Outline each Trypanosoma brucei.
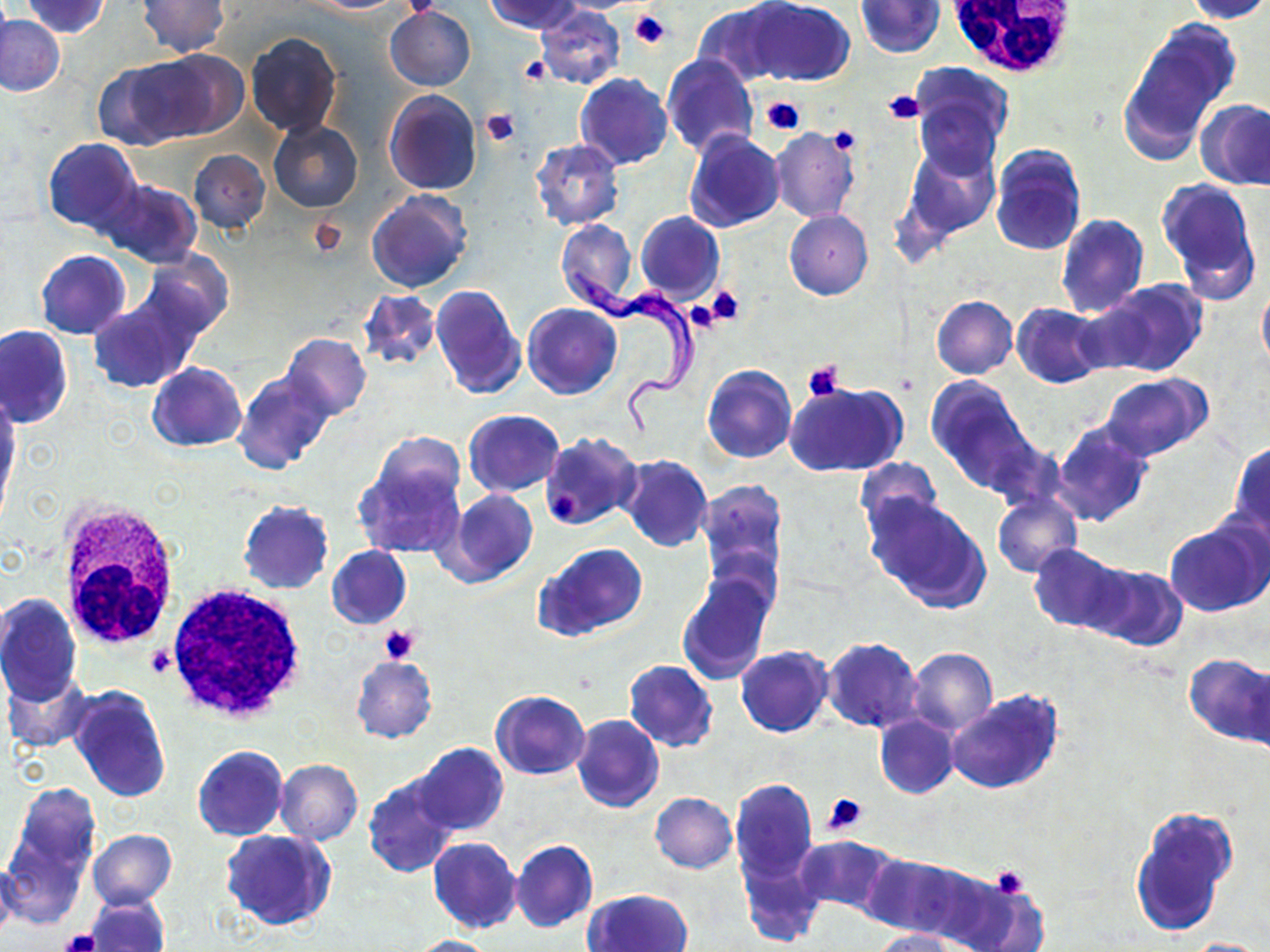
Approximate bounding boxes as [x1, y1, x2, y2] in pixels.
Trypanosoma brucei: [568, 267, 703, 444].

Platelet locations: [629, 7, 672, 50], [518, 56, 550, 85], [881, 89, 926, 124], [761, 96, 804, 136], [480, 108, 518, 147], [826, 126, 861, 156], [705, 285, 744, 327], [801, 359, 846, 402], [379, 625, 421, 666], [147, 645, 178, 679], [824, 792, 867, 834], [988, 865, 1031, 899], [59, 929, 100, 952]. White blood cell locations: [941, 0, 1085, 77], [55, 499, 183, 654], [166, 584, 308, 722]. Uninfected red blood cell locations: [20, 0, 111, 38], [311, 0, 402, 13], [485, 0, 583, 34], [747, 0, 854, 87], [855, 0, 944, 57], [1182, 0, 1270, 24], [137, 1, 230, 56], [694, 1, 793, 88], [535, 6, 625, 90], [624, 6, 674, 58], [385, 7, 475, 90], [1, 15, 65, 97], [1118, 18, 1240, 162], [246, 32, 342, 138], [128, 51, 244, 142], [661, 54, 756, 156], [93, 58, 197, 149], [909, 63, 1014, 155], [574, 73, 673, 171], [384, 89, 482, 194], [1196, 98, 1270, 190], [915, 99, 1001, 181], [268, 120, 364, 212], [770, 127, 860, 223], [684, 128, 785, 233], [42, 138, 141, 236], [531, 139, 624, 231], [901, 142, 1000, 246], [989, 145, 1086, 257], [187, 150, 271, 234], [1156, 179, 1261, 298], [99, 180, 202, 268], [366, 189, 473, 295], [784, 210, 873, 300], [635, 211, 724, 304], [1056, 213, 1148, 317], [556, 219, 639, 311], [35, 250, 130, 338], [138, 251, 231, 341], [1084, 278, 1208, 379], [431, 282, 526, 402], [1256, 283, 1270, 376], [357, 288, 440, 372], [87, 292, 202, 392], [931, 295, 1017, 379], [522, 303, 621, 399], [1012, 303, 1106, 388], [1, 326, 72, 428], [281, 334, 371, 420], [147, 361, 247, 451], [702, 365, 796, 465], [232, 370, 334, 474], [1099, 374, 1210, 462], [925, 378, 1040, 495], [784, 381, 908, 477], [0, 396, 19, 508], [463, 409, 564, 497], [1052, 420, 1153, 528], [540, 431, 642, 529], [370, 433, 466, 517], [1229, 440, 1270, 544], [352, 450, 466, 562], [617, 455, 712, 552], [854, 458, 942, 543], [696, 480, 788, 589], [441, 489, 539, 587], [865, 493, 991, 614], [992, 493, 1082, 578], [238, 500, 335, 593], [1164, 517, 1269, 617], [1029, 542, 1128, 634], [536, 543, 648, 640], [326, 545, 411, 629], [1083, 562, 1187, 650], [676, 572, 772, 683], [0, 593, 82, 706], [821, 638, 924, 733], [735, 646, 833, 737], [906, 647, 998, 737], [1183, 654, 1270, 748], [350, 655, 438, 743], [624, 660, 717, 752], [1244, 663, 1270, 758], [3, 670, 92, 754], [70, 685, 171, 801], [490, 689, 591, 779], [946, 689, 1063, 795], [572, 714, 664, 813], [875, 715, 958, 799], [409, 743, 509, 837], [193, 745, 288, 841], [275, 759, 362, 845], [363, 775, 459, 878], [730, 779, 817, 882], [2, 785, 98, 918], [650, 793, 738, 873], [1129, 804, 1239, 936], [87, 829, 176, 910], [220, 830, 336, 931], [794, 835, 899, 917], [427, 838, 521, 933], [511, 840, 598, 932], [739, 849, 824, 947], [864, 853, 972, 938], [0, 857, 21, 946], [942, 868, 1043, 952], [585, 888, 693, 952], [85, 895, 168, 952], [868, 929, 957, 952], [408, 935, 498, 952], [1181, 937, 1268, 951]. Slide-level diagnosis: Trypanosoma brucei. Light microscopy. Image is 1270×952 pixels. Thin blood smear. May-Grünwald-Giemsa-stained preparation. 1000x magnification. One field of a larger specimen.